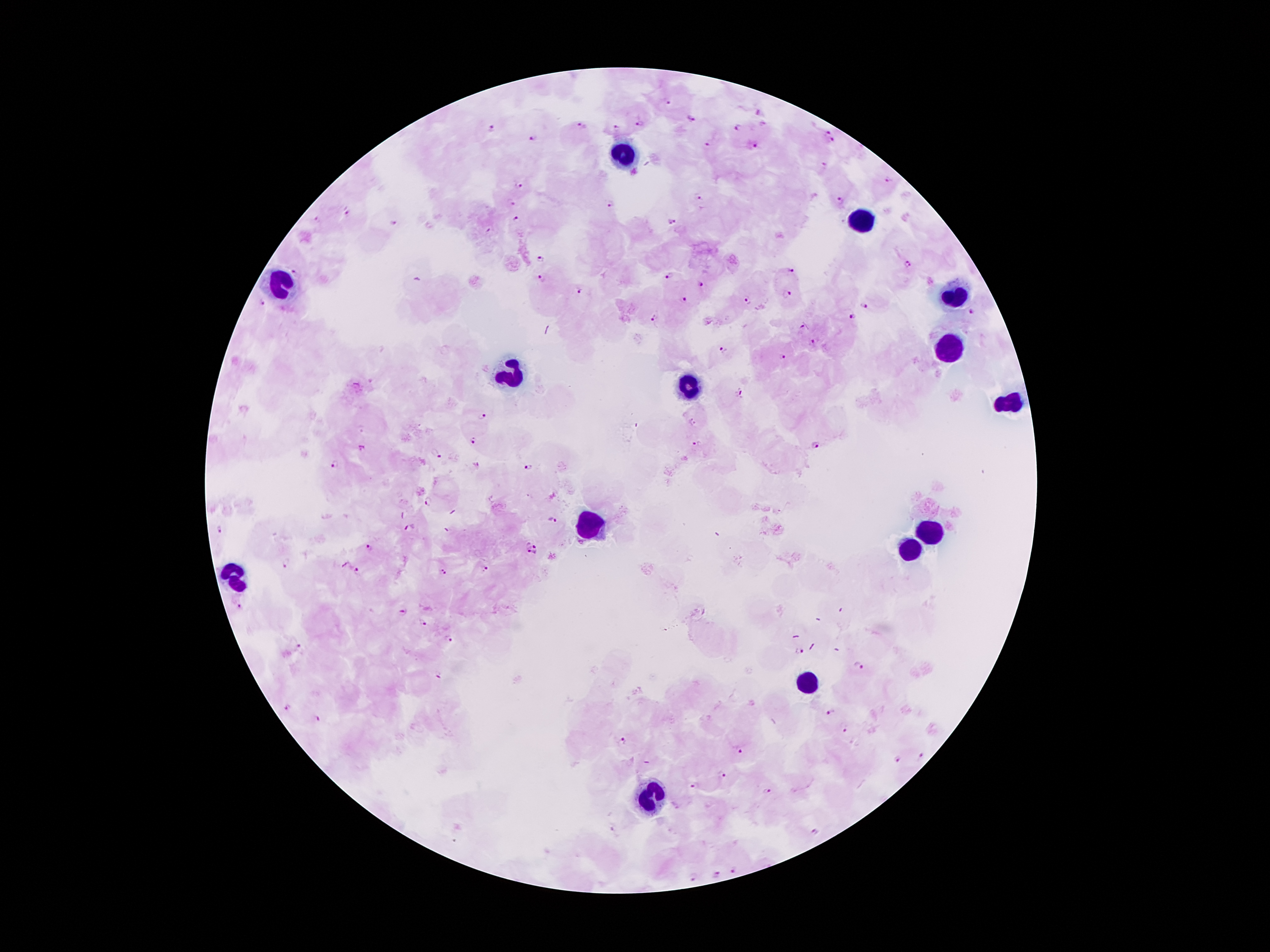

Approximate centers as {x, y} in pixels.
Summary:
  - Plasmodium parasite locations: {667, 103}, {693, 119}, {640, 124}, {581, 127}, {492, 128}, {616, 128}, {738, 128}, {826, 132}, {534, 137}, {832, 141}, {708, 146}, {754, 146}, {888, 181}, {520, 186}, {698, 196}, {839, 201}, {512, 202}, {610, 204}, {348, 214}, {318, 220}, {517, 221}, {670, 222}, {394, 223}, {540, 259}, {907, 264}, {791, 270}, {296, 271}, {670, 276}, {540, 279}, {700, 284}, {581, 292}, {788, 295}, {748, 299}, {684, 300}, {260, 302}, {863, 307}, {972, 314}, {853, 317}, {654, 318}, {801, 329}, {813, 344}, {723, 350}, {784, 356}, {740, 394}, {484, 415}, {693, 422}, {472, 441}, {696, 443}, {815, 445}, {438, 455}, {336, 464}, {528, 468}, {428, 502}, {551, 522}, {408, 528}, {217, 529}, {369, 548}, {527, 550}, {537, 550}, {286, 563}, {346, 564}, {484, 568}, {357, 571}, {443, 573}, {240, 606}, {402, 613}, {423, 623}, {448, 640}, {299, 647}, {799, 651}, {858, 665}, {438, 675}, {831, 712}, {319, 717}, {843, 729}, {622, 741}, {739, 751}, {920, 756}, {898, 759}, {723, 774}, {694, 785}, {767, 791}, {814, 832}, {733, 870}, {715, 874}, {695, 877}
  - Leukocyte locations: {621, 155}, {862, 222}, {276, 286}, {955, 301}, {948, 350}, {513, 375}, {688, 386}, {1008, 401}, {584, 524}, {929, 530}, {909, 545}, {234, 575}, {809, 684}, {650, 799}
  - Magnification: 100x
  - Patient malaria status: infected with Plasmodium falciparum
  - Field of view: single
  - Preparation: thick blood smear
  - Image size: 1270×952 pixels
  - Capture: smartphone through the microscope eyepiece
  - Stain: Giemsa